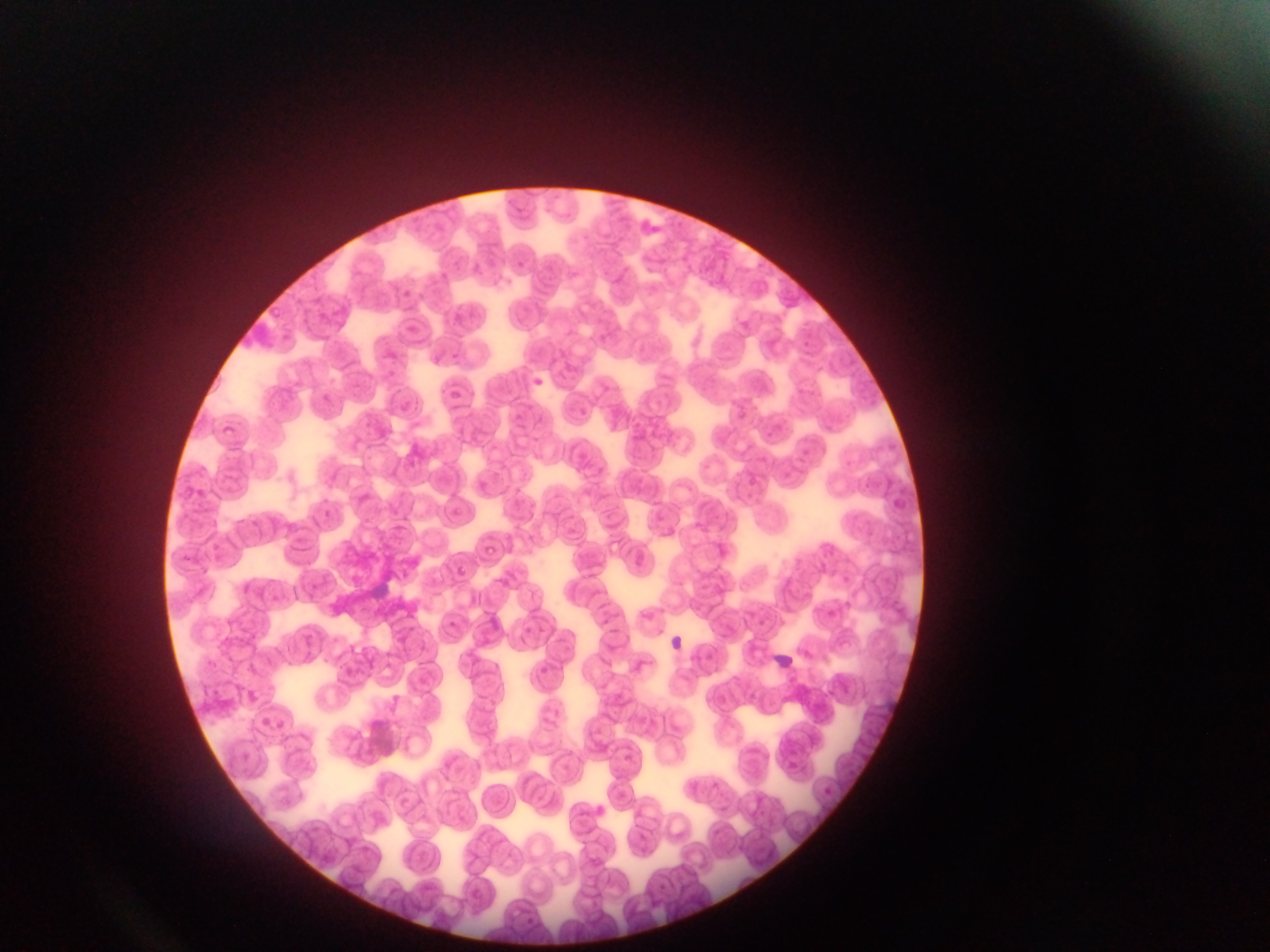 Approximate bounding boxes as [left, top, right, bottom] in pixels. Leukocyte locations: [667, 635, 686, 652], [774, 650, 795, 669]. Thin blood smear. One field of view. Sample from Ghana. Image is 1270×952 pixels. Photographed through a microscope with a mobile-phone camera.